Locate every Plasmodium falciparum-infected red blood cell.
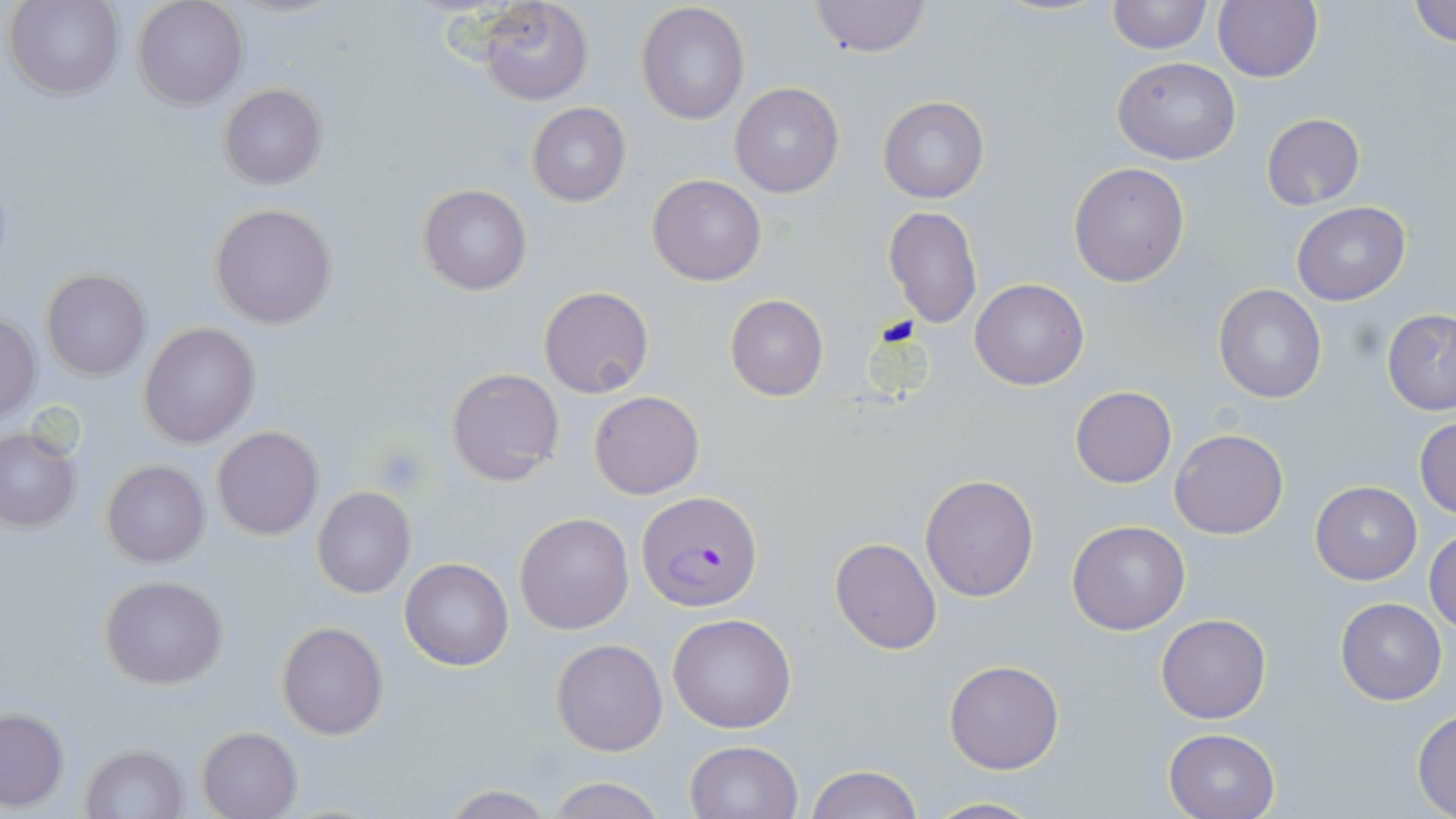

Approximate bounding boxes as (x1,y1)-(x2,y2) corner pairs in pixels.
Plasmodium falciparum-infected red blood cells: (637,490)-(763,613).

Uninfected red blood cell locations: (132,0)-(247,110), (478,0)-(596,106), (1107,0)-(1210,55), (1213,0)-(1323,84), (1410,0)-(1456,49), (5,1)-(125,101), (809,1)-(930,57), (635,2)-(751,125), (1112,56)-(1240,165), (730,83)-(844,199), (219,84)-(327,189), (878,96)-(988,203), (526,103)-(631,206), (1262,112)-(1366,210), (1068,162)-(1189,287), (648,174)-(766,285), (418,184)-(531,296), (1291,202)-(1411,306), (210,203)-(338,328), (884,206)-(982,327), (41,268)-(151,380), (969,278)-(1089,390), (1213,284)-(1326,403), (539,285)-(654,398), (725,294)-(829,402), (1382,309)-(1456,416), (0,311)-(41,424), (139,322)-(261,448), (446,365)-(565,486), (1070,385)-(1176,487), (589,390)-(705,499), (1414,416)-(1456,519), (211,426)-(324,541), (1171,428)-(1289,539), (1,429)-(81,531), (102,460)-(209,567), (918,473)-(1039,601), (1311,481)-(1422,584), (312,486)-(415,598), (515,511)-(635,634), (1067,519)-(1191,636), (1427,529)-(1456,634), (829,537)-(943,656), (401,557)-(514,671), (99,574)-(230,689), (1336,598)-(1446,704), (667,612)-(797,733), (1156,613)-(1271,724), (276,621)-(388,739), (552,638)-(668,756), (944,658)-(1064,774), (0,708)-(69,811), (1413,709)-(1456,816), (198,725)-(303,819), (1164,728)-(1279,818), (684,740)-(803,819), (82,742)-(189,817), (805,765)-(923,819), (545,776)-(666,819), (437,784)-(558,818), (924,796)-(1045,818). Platelet locations: (374,446)-(428,494). Slide-level diagnosis: Plasmodium falciparum. May-Grünwald-Giemsa stain. One field of a larger specimen. Image is 1456×819 pixels. Optical microscopy. Thin blood film. 1000x magnification.